Name the blood parasite species.
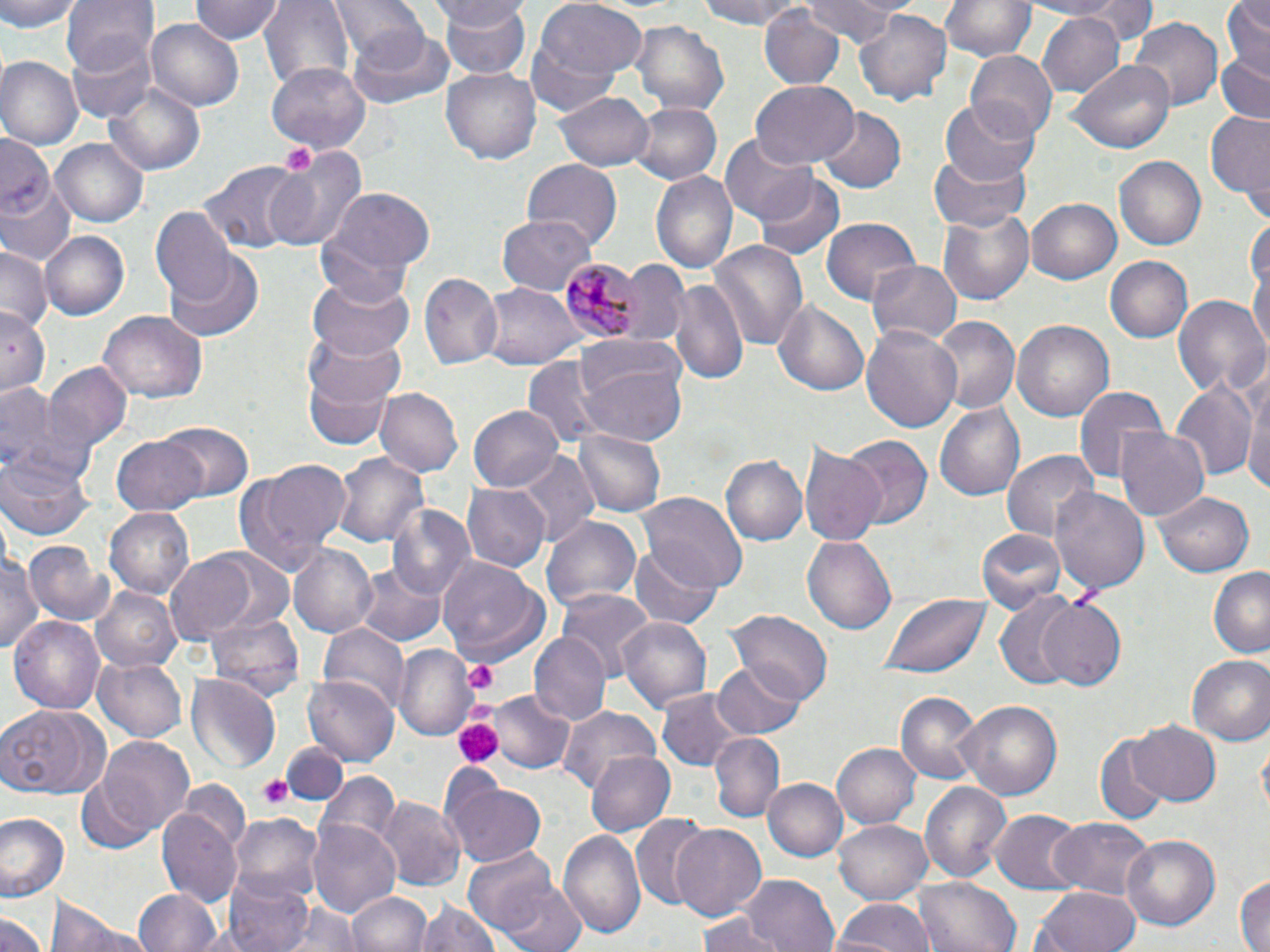
Plasmodium malariae.

Approximate bounding boxes as (x1, y1, x2, y2) in pixels. Uninfected red blood cell locations: (0, 0, 81, 33), (60, 0, 156, 78), (191, 0, 282, 45), (262, 0, 353, 91), (328, 0, 424, 60), (535, 0, 651, 84), (697, 0, 806, 30), (802, 0, 910, 45), (941, 0, 1034, 64), (1015, 0, 1128, 19), (1076, 0, 1155, 46), (1219, 0, 1270, 78), (437, 1, 531, 77), (758, 5, 845, 90), (854, 7, 955, 105), (1036, 10, 1126, 99), (1124, 15, 1225, 113), (147, 19, 245, 112), (627, 20, 728, 115), (528, 25, 630, 117), (346, 27, 456, 110), (68, 29, 155, 120), (964, 50, 1056, 139), (1212, 51, 1270, 125), (0, 57, 81, 152), (1071, 60, 1174, 154), (267, 62, 371, 152), (442, 65, 543, 165), (104, 80, 207, 176), (749, 81, 857, 170), (555, 89, 657, 171), (940, 99, 1039, 187), (630, 102, 720, 184), (816, 107, 905, 193), (1204, 111, 1269, 201), (1, 130, 56, 236), (720, 131, 820, 223), (52, 138, 147, 226), (263, 147, 368, 253), (926, 149, 1030, 234), (1115, 155, 1208, 251), (522, 159, 624, 248), (0, 161, 77, 269), (200, 161, 303, 253), (649, 169, 737, 273), (755, 174, 845, 261), (322, 188, 436, 279), (1026, 199, 1120, 285), (937, 205, 1037, 306), (151, 209, 239, 308), (498, 212, 595, 296), (314, 218, 423, 308), (822, 218, 921, 305), (41, 230, 129, 321), (1250, 238, 1270, 361), (707, 239, 810, 352), (0, 244, 52, 334), (164, 251, 265, 344), (1105, 253, 1193, 341), (866, 257, 961, 345), (623, 260, 692, 345), (420, 273, 505, 369), (304, 275, 413, 366), (671, 277, 751, 386), (482, 283, 580, 372), (1171, 293, 1268, 401), (771, 296, 870, 397), (0, 309, 50, 398), (100, 312, 206, 404), (930, 315, 1020, 415), (1012, 319, 1116, 423), (861, 324, 963, 435), (303, 328, 406, 413), (575, 344, 686, 446), (522, 357, 608, 451), (299, 358, 401, 451), (42, 362, 132, 454), (1241, 370, 1270, 506), (1170, 376, 1260, 480), (0, 382, 82, 483), (1073, 386, 1170, 488), (374, 389, 462, 479), (933, 403, 1027, 503), (470, 405, 563, 492), (157, 424, 254, 503), (1115, 425, 1212, 524), (574, 427, 666, 516), (839, 434, 933, 533), (111, 435, 210, 515), (800, 442, 887, 544), (1002, 450, 1101, 549), (0, 451, 96, 542), (514, 451, 598, 544), (332, 452, 427, 548), (723, 455, 810, 547), (232, 458, 352, 574), (463, 485, 548, 573), (1051, 487, 1150, 599), (1153, 489, 1256, 576), (638, 492, 745, 592), (388, 505, 475, 603), (106, 508, 195, 599), (542, 512, 643, 616), (978, 526, 1067, 613), (803, 535, 897, 636), (0, 539, 41, 661), (25, 541, 113, 627), (631, 541, 721, 627), (289, 543, 381, 638), (163, 550, 264, 644), (439, 559, 548, 666), (355, 562, 446, 647), (1209, 566, 1270, 659), (90, 586, 181, 673), (555, 590, 655, 679), (879, 594, 993, 678), (993, 594, 1088, 691), (1036, 597, 1128, 688), (205, 609, 305, 702), (725, 610, 834, 705), (10, 615, 104, 715), (614, 615, 711, 712), (321, 623, 410, 713), (531, 632, 608, 723), (394, 644, 475, 739), (1185, 654, 1270, 744), (94, 657, 187, 742), (711, 663, 807, 737), (186, 672, 280, 771), (303, 675, 403, 766), (654, 684, 747, 772), (896, 691, 982, 786), (489, 692, 575, 774), (954, 699, 1062, 801), (0, 705, 110, 799), (560, 707, 663, 800), (1127, 720, 1219, 807), (709, 732, 782, 821), (1095, 733, 1175, 822), (98, 736, 197, 838), (281, 739, 345, 802), (833, 741, 920, 830), (585, 750, 674, 835), (315, 772, 400, 863), (446, 778, 547, 868), (761, 778, 845, 862), (77, 780, 152, 855), (179, 780, 250, 857), (921, 782, 1012, 883), (377, 796, 465, 891), (157, 805, 243, 907), (990, 809, 1082, 891), (0, 812, 69, 901), (232, 814, 323, 898), (631, 817, 717, 911), (834, 818, 933, 904), (1048, 818, 1152, 899), (310, 819, 402, 920), (671, 822, 767, 919), (559, 828, 646, 941), (1119, 834, 1221, 932), (465, 852, 586, 952), (739, 874, 841, 952), (223, 875, 316, 952), (1234, 875, 1268, 952), (914, 877, 1021, 952), (1033, 885, 1142, 952), (134, 889, 223, 952), (347, 891, 432, 952), (831, 897, 932, 952), (269, 898, 366, 952), (47, 899, 152, 952), (414, 899, 500, 952), (0, 908, 51, 952), (698, 914, 785, 952). Plasmodium malariae-infected red blood cell locations: (558, 260, 639, 340). Platelet locations: (278, 143, 317, 179), (464, 663, 499, 691), (461, 700, 497, 724), (457, 721, 501, 767), (257, 776, 291, 809). Image is 1270×952 pixels. Thin blood smear. May-Grünwald-Giemsa-stained preparation. Captured at 1000x magnification. One field of a larger specimen. Light microscopy.